Locate every parasitized red blood cell.
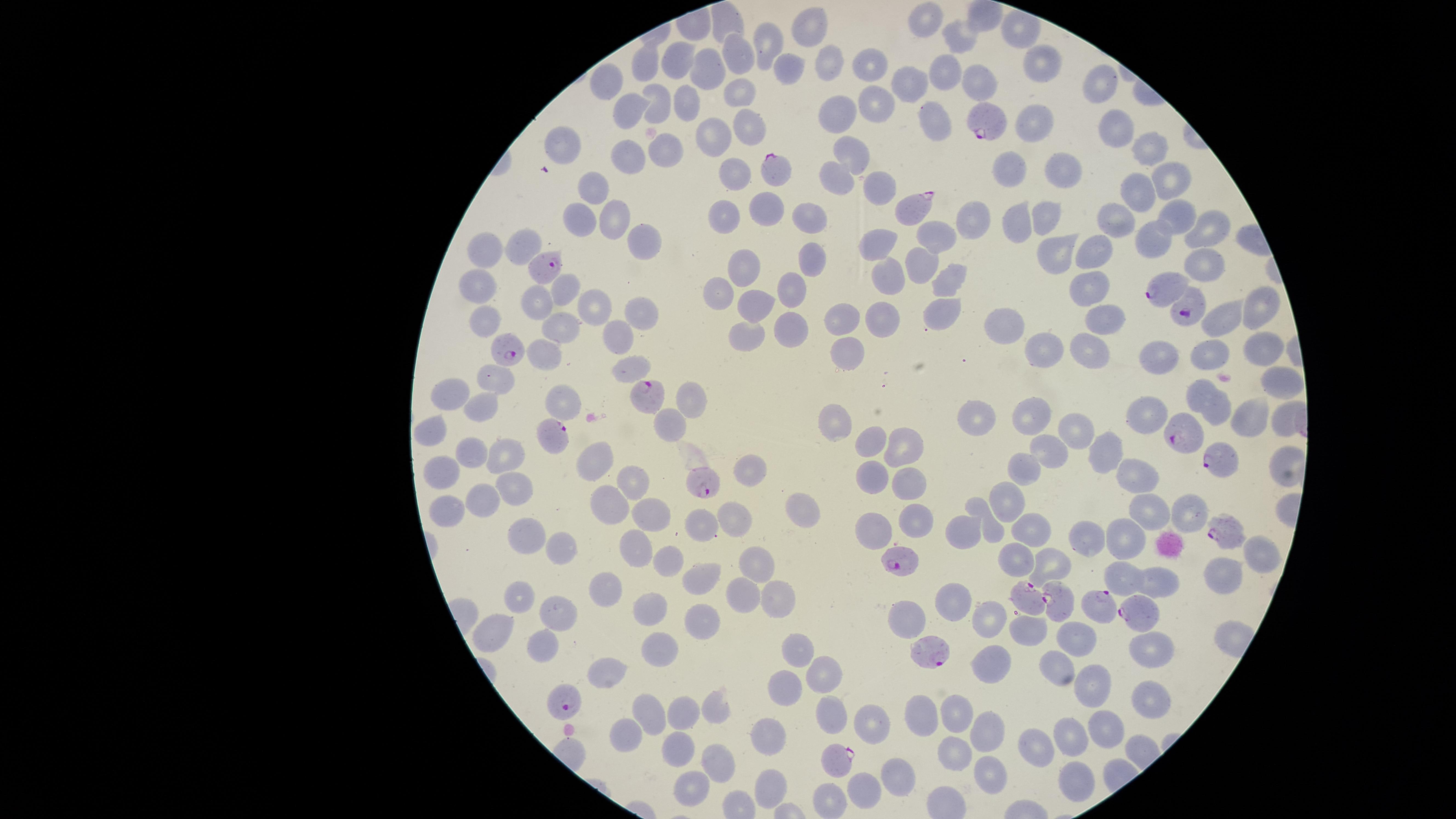
Approximate marker points as {x, y} in pixels.
Parasitized red blood cells: {986, 123}, {779, 165}, {914, 207}, {549, 267}, {1164, 290}, {1185, 307}, {510, 347}, {647, 398}, {1182, 429}, {548, 438}, {1220, 459}, {711, 477}, {1220, 530}, {904, 558}, {1030, 598}, {1059, 598}, {1098, 607}, {1138, 613}, {928, 649}, {568, 699}, {836, 762}.

Approximate marker points as {x, y} in pixels.
Summary:
  - Uninfected red blood cells: {926, 19}, {809, 24}, {961, 38}, {760, 45}, {735, 53}, {684, 56}, {647, 61}, {789, 63}, {869, 63}, {829, 65}, {1042, 65}, {710, 67}, {945, 69}, {611, 80}, {977, 81}, {1100, 82}, {912, 84}, {741, 96}, {872, 100}, {660, 103}, {685, 103}, {633, 106}, {838, 112}, {938, 119}, {1035, 122}, {747, 126}, {1115, 126}, {715, 138}, {567, 141}, {664, 144}, {853, 146}, {1150, 146}, {631, 152}, {1016, 169}, {1068, 169}, {843, 172}, {731, 175}, {880, 177}, {1168, 180}, {587, 185}, {1142, 189}, {775, 210}, {1051, 211}, {616, 212}, {575, 213}, {723, 213}, {971, 213}, {1122, 214}, {1172, 214}, {814, 219}, {1020, 223}, {1206, 229}, {939, 231}, {1155, 236}, {646, 241}, {527, 244}, {1058, 245}, {880, 248}, {485, 251}, {1088, 256}, {818, 260}, {1205, 260}, {927, 261}, {746, 269}, {953, 276}, {897, 281}, {1090, 285}, {479, 287}, {565, 289}, {794, 290}, {723, 292}, {535, 301}, {760, 302}, {594, 304}, {943, 306}, {1263, 306}, {888, 310}, {636, 312}, {1105, 315}, {487, 319}, {843, 319}, {1226, 320}, {556, 325}, {798, 327}, {1005, 331}, {751, 337}, {622, 338}, {1255, 345}, {1041, 349}, {1093, 349}, {1150, 350}, {851, 351}, {1205, 351}, {550, 354}, {630, 364}, {1280, 377}, {496, 380}, {1202, 389}, {453, 394}, {555, 397}, {695, 398}, {483, 405}, {1150, 411}, {1218, 415}, {836, 417}, {975, 418}, {1028, 419}, {1251, 420}, {1280, 420}, {668, 421}, {432, 426}, {1075, 427}, {871, 440}, {907, 443}, {475, 450}, {1103, 450}, {1053, 451}, {511, 456}, {596, 464}, {1027, 467}, {749, 468}, {447, 474}, {871, 476}, {1142, 479}, {632, 480}, {909, 481}, {511, 489}, {1007, 491}, {480, 497}, {613, 504}, {802, 508}, {1147, 510}, {452, 512}, {652, 514}, {730, 516}, {1185, 516}, {915, 518}, {699, 522}, {960, 528}, {1031, 528}, {877, 530}, {989, 531}, {532, 532}, {1090, 535}, {1128, 536}, {555, 547}, {636, 548}, {1015, 553}, {668, 558}, {1259, 561}, {759, 563}, {1048, 564}, {706, 574}, {1227, 576}, {1126, 579}, {1166, 583}, {616, 588}, {745, 589}, {775, 593}, {524, 594}, {955, 594}, {649, 606}, {558, 616}, {710, 616}, {908, 617}, {987, 617}, {500, 628}, {1027, 635}, {1080, 636}, {549, 642}, {1148, 643}, {798, 651}, {663, 652}, {1061, 660}, {612, 670}, {825, 671}, {989, 671}, {781, 687}, {1103, 693}, {1151, 693}, {718, 704}, {649, 708}, {687, 708}, {835, 713}, {921, 713}, {958, 715}, {1110, 722}, {872, 727}, {987, 730}, {622, 734}, {772, 735}, {1075, 740}, {682, 749}, {1032, 751}, {951, 755}, {721, 768}, {993, 773}, {897, 776}, {769, 781}, {1077, 782}, {689, 785}, {864, 791}, {833, 797}
  - Stain: Giemsa
  - Field of view: single
  - Capture: smartphone photograph through the microscope eyepiece
  - Image size: 1456×819 pixels
  - Preparation: thin blood smear
  - Species: Plasmodium falciparum
  - Visible region: circular